Classify this cell by malaria status.
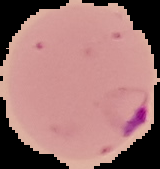

Parasitized.

image_size: 160×169 pixels
image_type: cell region segmented out of the field of view; surrounding area masked to black
preparation: thin blood film